Describe the morphology of the erythrocytes.
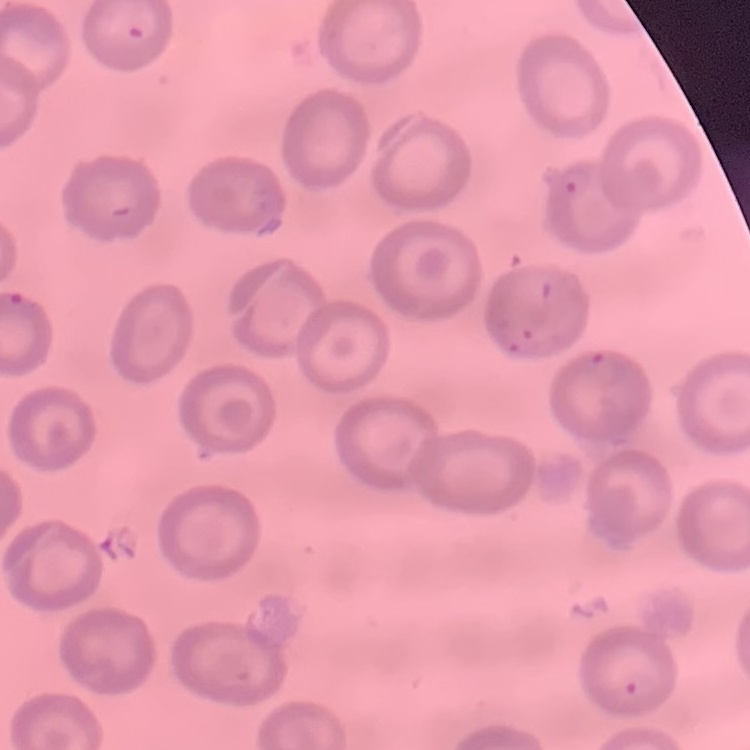

No rouleaux formation.

Summary:
  - Preparation: thin blood film
  - Stain: Field's or Giemsa
  - Image type: square crop of a larger photomicrograph